Locate every blood parasite and identify its species.
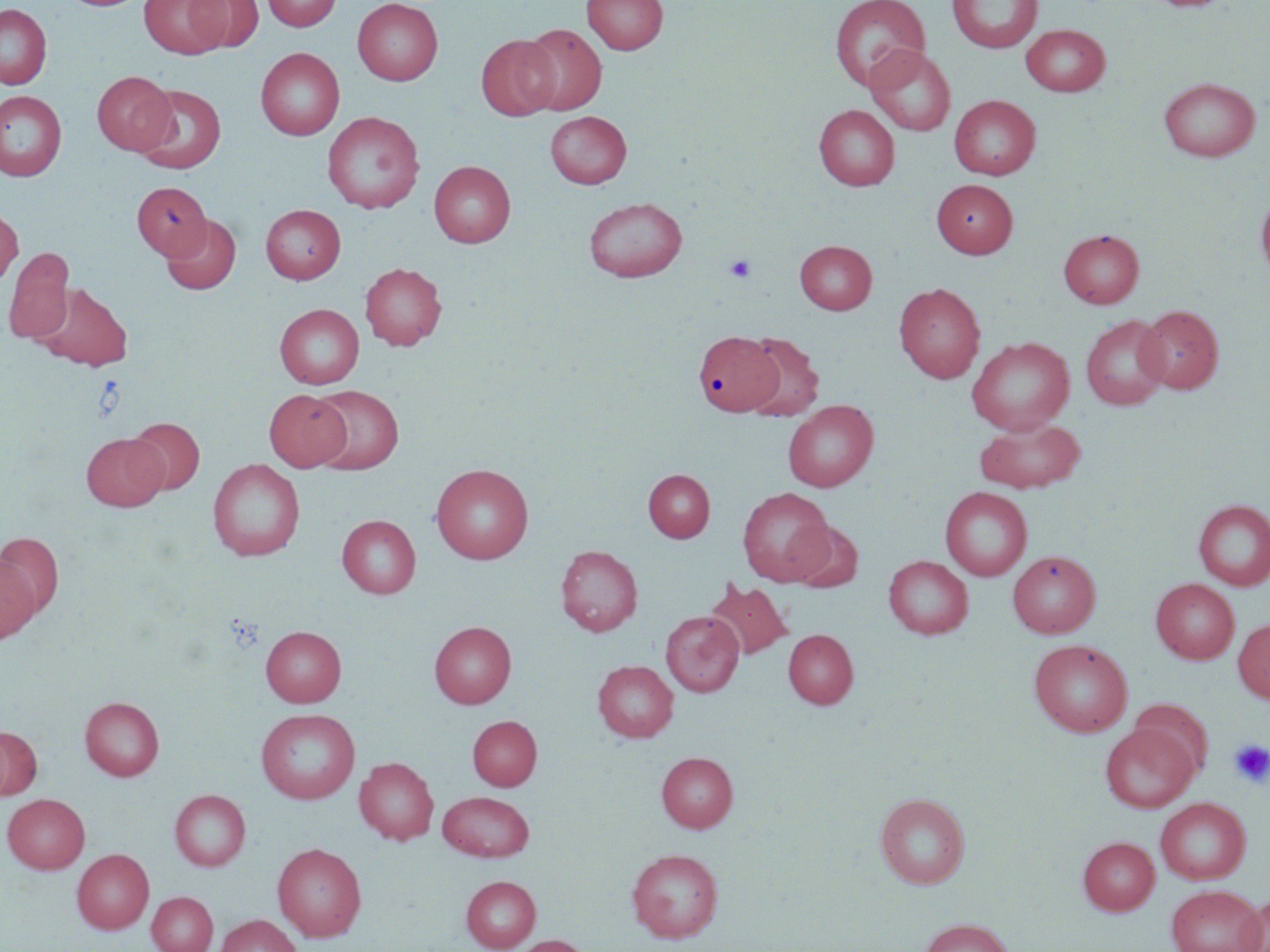
No blood parasites seen.

Summary:
  - Coordinate format: approximate bounding boxes as (x1, y1, x2, y2) in pixels
  - Platelet locations: (723, 254, 757, 283), (1229, 739, 1270, 788)
  - Uninfected red blood cell locations: (140, 0, 230, 59), (185, 0, 263, 52), (262, 0, 341, 31), (353, 0, 443, 85), (582, 0, 668, 55), (947, 0, 1042, 53), (1142, 0, 1235, 12), (829, 1, 930, 90), (0, 3, 51, 89), (1021, 23, 1111, 96), (520, 24, 606, 114), (476, 34, 560, 120), (865, 45, 955, 135), (256, 47, 344, 140), (92, 70, 177, 155), (1158, 77, 1260, 161), (134, 85, 225, 174), (0, 91, 66, 181), (949, 95, 1041, 180), (814, 104, 900, 191), (322, 111, 424, 213), (545, 111, 632, 189), (429, 161, 515, 247), (931, 178, 1017, 258), (132, 182, 210, 260), (1256, 189, 1270, 285), (583, 197, 687, 282), (261, 204, 346, 284), (0, 206, 22, 289), (160, 214, 241, 294), (1058, 229, 1144, 308), (794, 240, 877, 314), (5, 250, 75, 343), (360, 262, 447, 350), (34, 282, 133, 370), (894, 282, 985, 383), (275, 303, 364, 389), (1136, 305, 1224, 394), (1081, 314, 1171, 410), (693, 331, 783, 417), (741, 333, 823, 420), (966, 337, 1075, 434), (308, 385, 404, 473), (263, 389, 350, 471), (783, 400, 878, 492), (974, 416, 1085, 494), (127, 417, 204, 494), (81, 433, 167, 511), (208, 458, 305, 561), (431, 463, 534, 563), (643, 469, 714, 542), (940, 486, 1032, 581), (737, 487, 834, 585), (1194, 499, 1270, 590), (337, 515, 421, 598), (787, 521, 863, 592), (0, 532, 64, 619), (555, 545, 643, 636), (1007, 550, 1101, 638), (0, 554, 40, 645), (883, 555, 973, 639), (1150, 578, 1239, 664), (704, 580, 792, 661), (661, 611, 744, 696), (1233, 618, 1270, 703), (429, 621, 516, 708), (261, 626, 346, 706), (783, 629, 858, 708), (1029, 639, 1133, 737), (593, 660, 678, 742), (80, 696, 164, 780), (1128, 700, 1212, 779), (256, 708, 359, 803), (468, 715, 542, 790), (1100, 723, 1198, 812), (0, 726, 41, 800), (657, 751, 738, 832), (354, 757, 439, 844), (170, 789, 251, 870), (438, 791, 534, 861), (875, 792, 970, 889), (2, 793, 90, 873), (1155, 797, 1251, 884), (1078, 836, 1160, 915), (272, 842, 367, 941), (627, 848, 723, 942), (72, 849, 153, 934), (461, 875, 541, 951), (1166, 884, 1266, 952), (147, 891, 218, 952), (1236, 896, 1270, 952), (215, 914, 301, 952), (919, 918, 1015, 952), (510, 935, 591, 952)
  - Slide-level diagnosis: negative for blood parasites
  - Preparation: thin blood film
  - Stain: May-Grünwald-Giemsa
  - Field of view: single
  - Modality: light microscopy
  - Image size: 1270×952 pixels
  - Magnification: 1000x